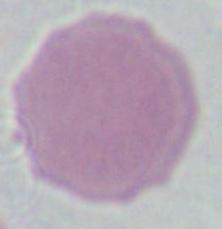 Photomicrograph. Captured at 1000x magnification. An erythrocyte is shown.